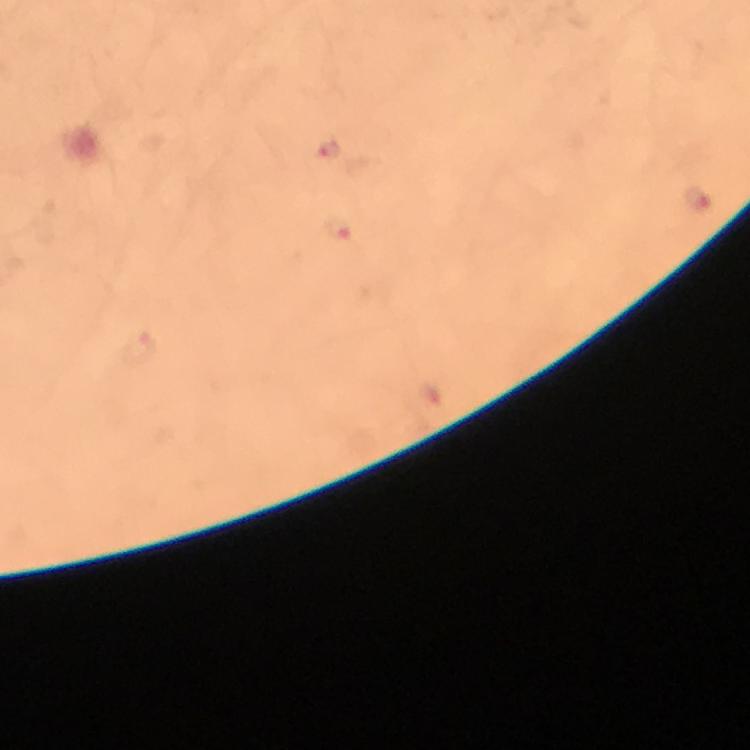 Approximate centers as [x, y] in pixels. Malaria parasite locations: [327, 150], [697, 198], [338, 229]. Immersion oil was used. Thick smear. Giemsa stain. Cropped region of a single field of view. From a malaria diagnostic workup. Photographed through the microscope with a smartphone camera. At 100x magnification. Image is 750×750 pixels.